Describe the morphology of the red blood cells.
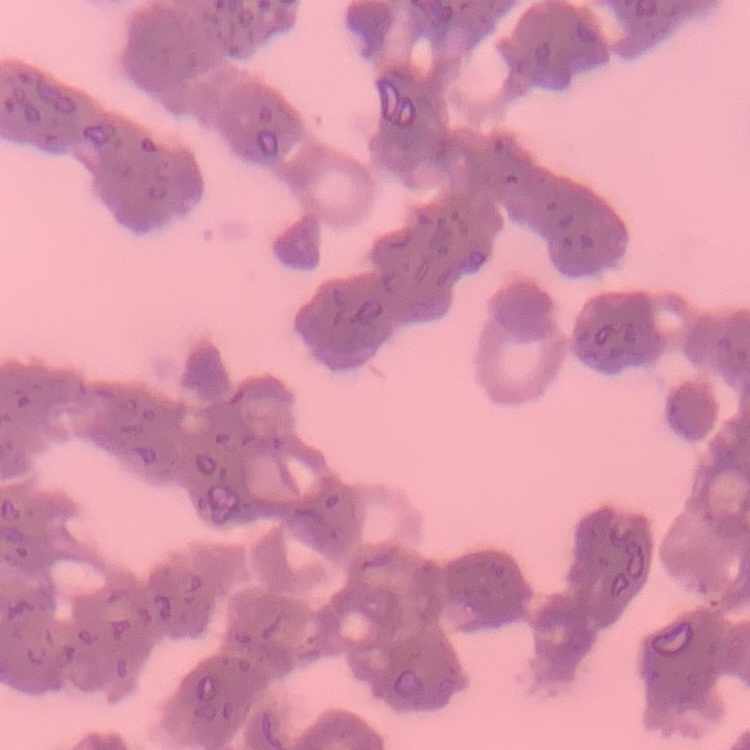
They show rouleaux formation.

One tile cut from a larger photomicrograph. Thin peripheral smear. Field's or Giemsa stain.